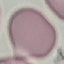 Malaria status: uninfected. Cell patch, automatically extracted from a larger field of view and resized to 64 × 64 pixels. Thin blood film. Photographed with a smartphone camera at the microscope eyepiece. Giemsa stain.